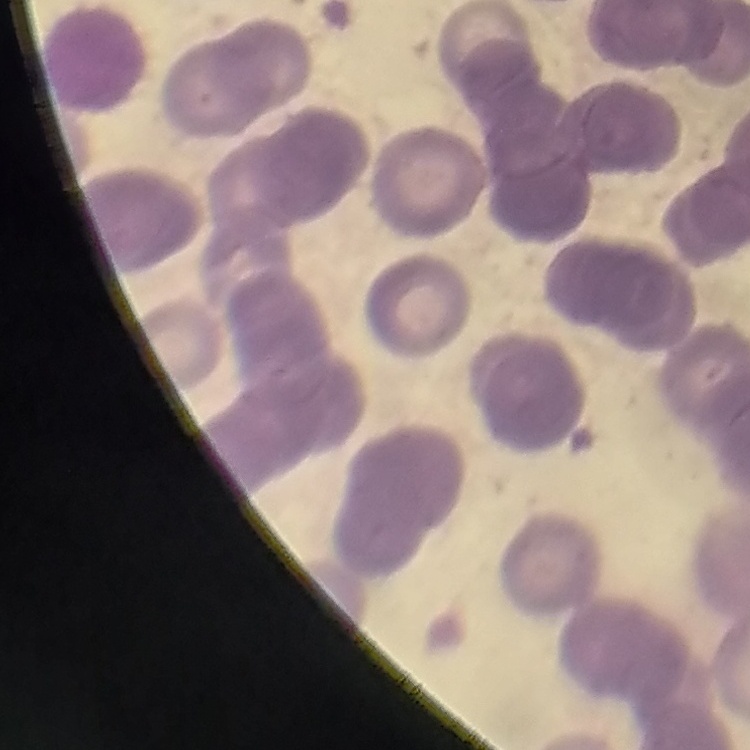
red blood cell morphology = rouleaux formation
stain = Field's or Giemsa
image type = square crop of a larger photomicrograph
preparation = thin peripheral smear